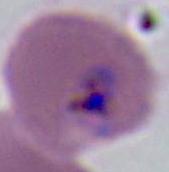
A Plasmodium parasite is shown. Micrograph. Captured at either 400x or 1000x magnification.